Report the malaria status of this cell.
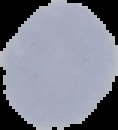

Uninfected.

image size = 118×130 pixels
image type = segmented cell region on a black background
preparation = thin blood smear